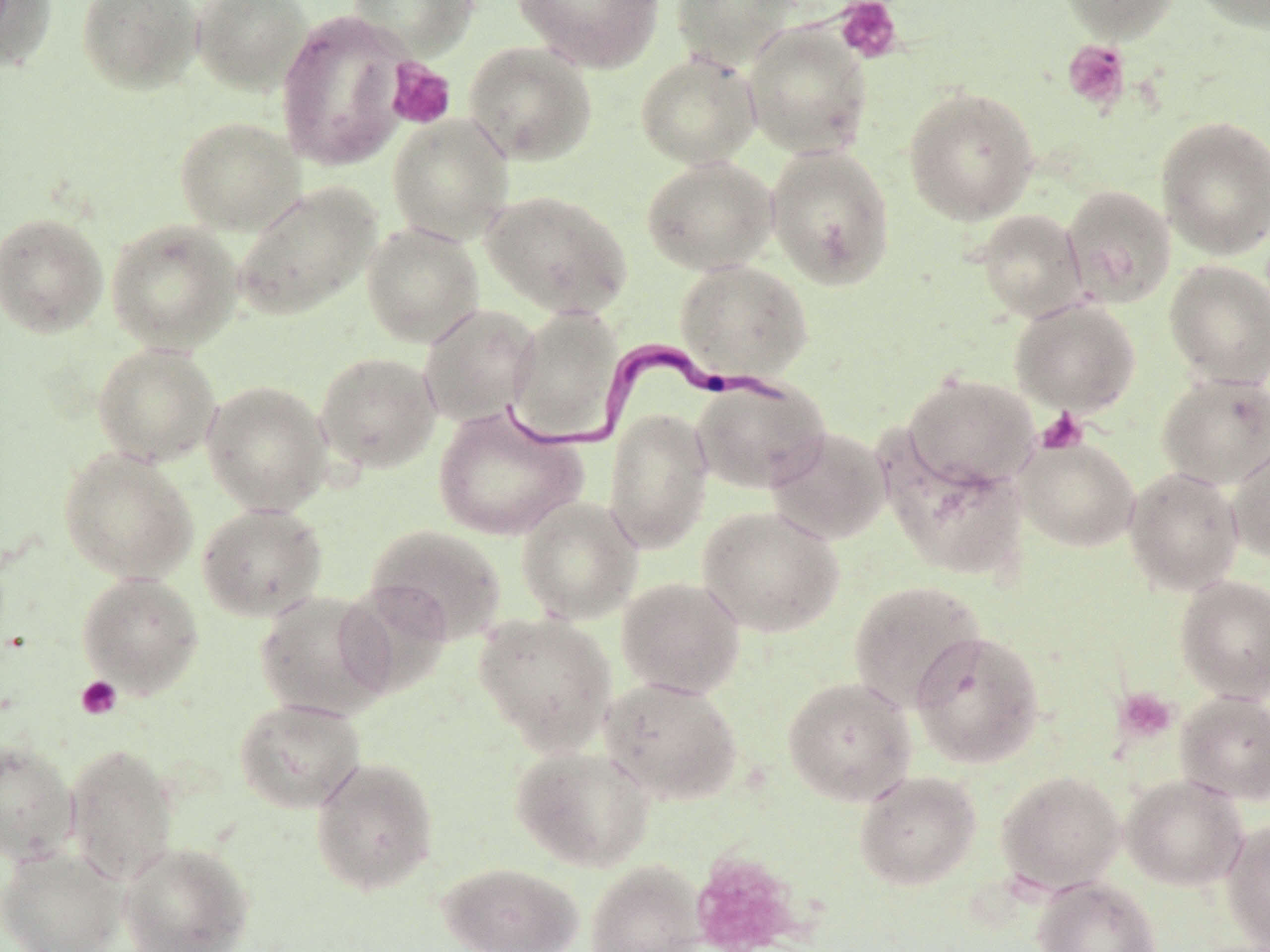

slide_level_diagnosis: Trypanosoma brucei
field_of_view: single
platelet_locations: 'approximate bounding boxes as named x1/y1/x2/y2 corners in pixels: (x1=835, y1=0, x2=903, y2=63), (x1=1062, y1=40, x2=1130, y2=110), (x1=386, y1=58, x2=456, y2=130), (x1=1036, y1=408, x2=1088, y2=454), (x1=76, y1=676, x2=122, y2=720), (x1=1114, y1=687, x2=1177, y2=743), (x1=691, y1=852, x2=803, y2=952)'
modality: light microscopy
trypanosoma_brucei_locations: 'approximate bounding boxes as named x1/y1/x2/y2 corners in pixels: (x1=503, y1=340, x2=790, y2=461)'
stain: May-Grünwald-Giemsa
image_size: 1270×952 pixels
uninfected_red_blood_cell_locations: 'approximate bounding boxes as named x1/y1/x2/y2 corners in pixels: (x1=0, y1=0, x2=57, y2=71), (x1=76, y1=0, x2=204, y2=94), (x1=191, y1=0, x2=311, y2=95), (x1=348, y1=0, x2=478, y2=60), (x1=513, y1=0, x2=665, y2=72), (x1=672, y1=0, x2=800, y2=70), (x1=1056, y1=0, x2=1180, y2=43), (x1=1188, y1=0, x2=1270, y2=33), (x1=275, y1=10, x2=414, y2=171), (x1=742, y1=22, x2=872, y2=159), (x1=464, y1=42, x2=598, y2=166), (x1=635, y1=52, x2=761, y2=169), (x1=903, y1=86, x2=1040, y2=224), (x1=388, y1=114, x2=514, y2=244), (x1=174, y1=116, x2=305, y2=235), (x1=1156, y1=116, x2=1270, y2=260), (x1=764, y1=144, x2=897, y2=290), (x1=641, y1=156, x2=778, y2=275), (x1=232, y1=182, x2=380, y2=320), (x1=1062, y1=184, x2=1177, y2=308), (x1=482, y1=189, x2=633, y2=319), (x1=976, y1=209, x2=1087, y2=322), (x1=0, y1=212, x2=108, y2=338), (x1=106, y1=219, x2=243, y2=353), (x1=361, y1=222, x2=484, y2=347), (x1=675, y1=259, x2=813, y2=382), (x1=1164, y1=260, x2=1270, y2=388), (x1=1010, y1=297, x2=1141, y2=417), (x1=418, y1=304, x2=541, y2=426), (x1=507, y1=305, x2=623, y2=443), (x1=92, y1=343, x2=222, y2=467), (x1=315, y1=351, x2=442, y2=473), (x1=902, y1=372, x2=1040, y2=493), (x1=1156, y1=372, x2=1270, y2=490), (x1=691, y1=376, x2=831, y2=493), (x1=201, y1=379, x2=332, y2=516), (x1=433, y1=406, x2=586, y2=540), (x1=604, y1=408, x2=713, y2=553), (x1=766, y1=426, x2=890, y2=545), (x1=1015, y1=436, x2=1140, y2=552), (x1=1227, y1=440, x2=1270, y2=564), (x1=57, y1=447, x2=198, y2=583), (x1=888, y1=449, x2=1029, y2=580), (x1=1123, y1=466, x2=1244, y2=595), (x1=516, y1=495, x2=643, y2=624), (x1=196, y1=503, x2=328, y2=621), (x1=697, y1=505, x2=844, y2=637), (x1=365, y1=523, x2=507, y2=644), (x1=76, y1=572, x2=204, y2=696), (x1=1175, y1=574, x2=1270, y2=703), (x1=616, y1=576, x2=746, y2=698), (x1=848, y1=579, x2=986, y2=709), (x1=337, y1=581, x2=453, y2=699), (x1=255, y1=590, x2=394, y2=719), (x1=473, y1=612, x2=617, y2=754), (x1=909, y1=630, x2=1045, y2=768), (x1=600, y1=676, x2=743, y2=805), (x1=782, y1=676, x2=917, y2=805), (x1=1175, y1=691, x2=1270, y2=805), (x1=233, y1=697, x2=366, y2=814), (x1=0, y1=739, x2=80, y2=865), (x1=64, y1=742, x2=179, y2=885), (x1=509, y1=743, x2=655, y2=871), (x1=310, y1=755, x2=439, y2=897), (x1=996, y1=769, x2=1125, y2=893), (x1=854, y1=770, x2=982, y2=890), (x1=1120, y1=773, x2=1248, y2=891), (x1=1221, y1=819, x2=1270, y2=950), (x1=118, y1=840, x2=255, y2=952), (x1=0, y1=845, x2=127, y2=952), (x1=437, y1=861, x2=583, y2=952), (x1=585, y1=861, x2=706, y2=952), (x1=1033, y1=877, x2=1161, y2=952)'
preparation: thin blood smear
magnification: 1000x